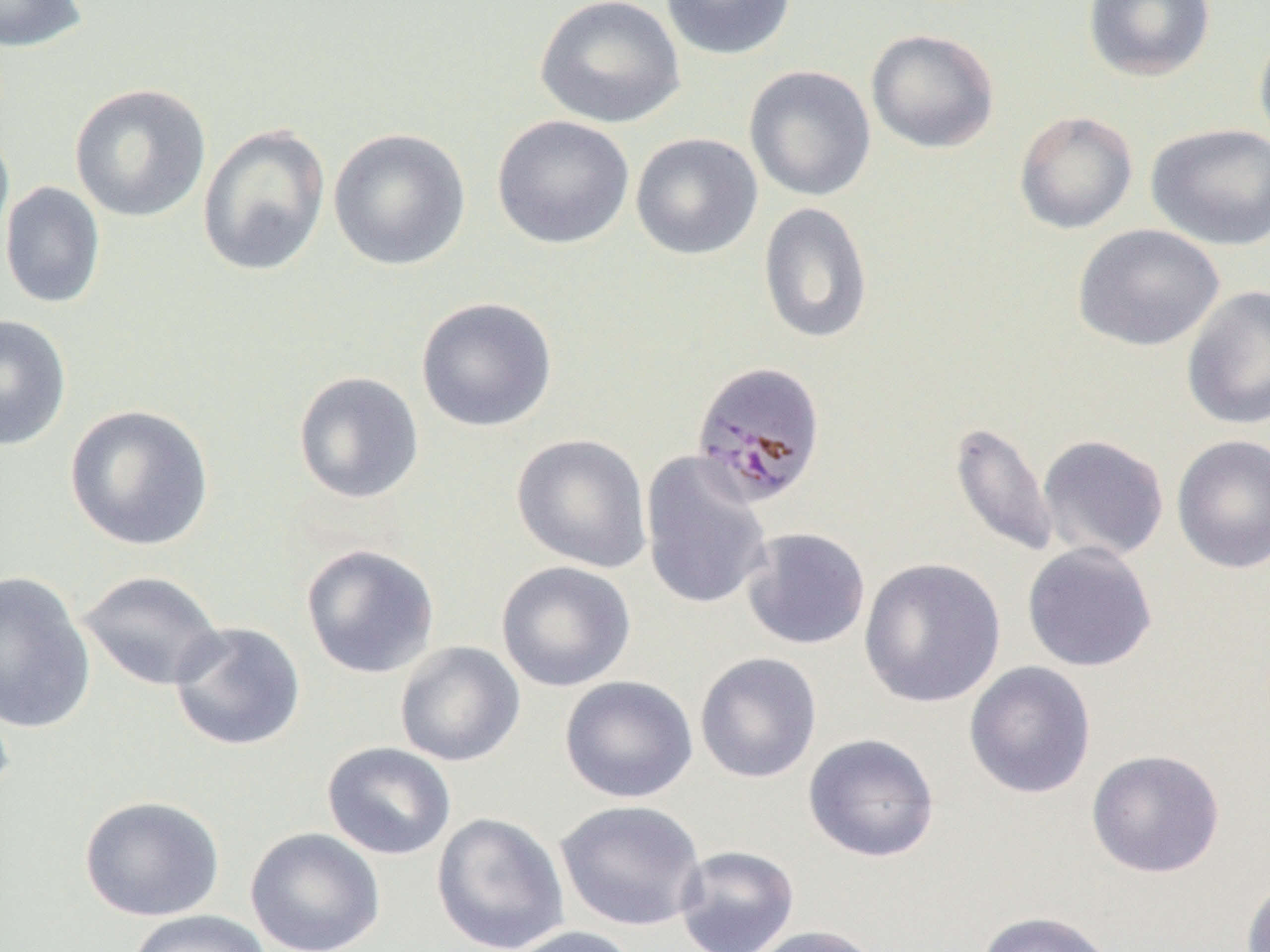
Summary:
  - Coordinate format: approximate bounding boxes as (x1,y1)-(x2,y2) corner pairs in pixels
  - Plasmodium malariae-infected red blood cell locations: (690,360)-(828,509)
  - Uninfected red blood cell locations: (0,0)-(89,53), (535,0)-(685,129), (660,0)-(797,60), (1083,0)-(1215,83), (1254,25)-(1270,153), (865,28)-(1000,154), (743,65)-(876,202), (69,83)-(212,223), (1013,110)-(1139,235), (491,114)-(635,250), (0,121)-(15,267), (196,123)-(331,278), (1145,123)-(1270,251), (328,127)-(471,272), (630,132)-(763,260), (0,181)-(106,309), (758,202)-(873,345), (1073,224)-(1225,352), (1181,285)-(1270,431), (415,297)-(558,432), (0,314)-(72,451), (292,371)-(425,505), (63,404)-(215,552), (948,421)-(1059,559), (511,433)-(653,573), (1037,434)-(1170,562), (1171,434)-(1270,574), (639,451)-(773,611), (739,527)-(871,651), (1021,542)-(1157,672), (300,543)-(440,679), (858,557)-(1006,708), (496,560)-(636,692), (0,570)-(96,734), (77,570)-(225,691), (168,621)-(307,752), (394,640)-(526,767), (694,652)-(822,784), (963,661)-(1097,799), (559,675)-(698,803), (0,688)-(15,809), (803,733)-(940,863), (321,742)-(456,861), (1085,748)-(1225,878), (79,795)-(225,922), (555,799)-(707,932), (431,812)-(570,952), (245,828)-(386,952), (674,845)-(800,952), (1240,874)-(1270,952), (124,909)-(274,952), (973,910)-(1118,952), (745,924)-(888,952), (505,925)-(640,952)
  - Slide-level diagnosis: Plasmodium malariae
  - Preparation: thin blood film
  - Image size: 1270×952 pixels
  - Modality: optical microscopy
  - Magnification: 1000x
  - Field of view: one of a larger specimen